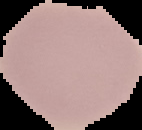

preparation = thin blood film
result = no Plasmodium parasites detected
image size = 142×130 pixels
image type = segmented cell region with the area outside set to black